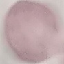 Malaria status: uninfected. Thin blood smear. Automatically extracted cell patch, resized to 64 × 64 pixels. Giemsa-stained preparation. Acquired by smartphone through the microscope eyepiece.